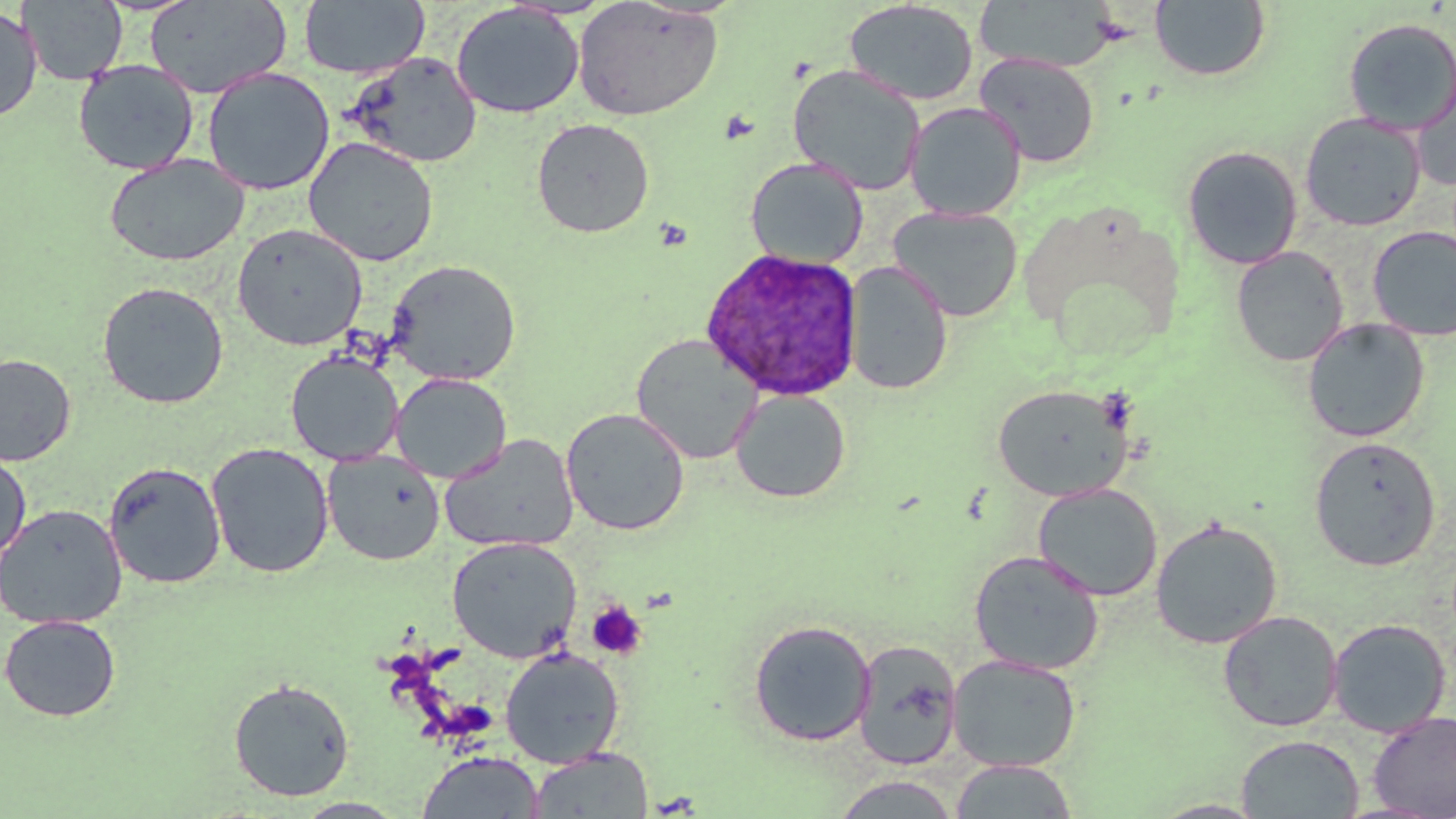
Approximate bounding boxes as named x1/y1/x2/y2 corners in pixels. Uninfected red blood cell locations: (x1=19, y1=0, x2=127, y2=86), (x1=300, y1=0, x2=429, y2=79), (x1=571, y1=0, x2=724, y2=121), (x1=1149, y1=0, x2=1271, y2=81), (x1=145, y1=1, x2=290, y2=98), (x1=843, y1=1, x2=979, y2=106), (x1=973, y1=1, x2=1121, y2=74), (x1=451, y1=3, x2=585, y2=119), (x1=0, y1=7, x2=42, y2=123), (x1=1342, y1=17, x2=1456, y2=134), (x1=347, y1=52, x2=482, y2=168), (x1=975, y1=53, x2=1099, y2=168), (x1=73, y1=59, x2=199, y2=175), (x1=1411, y1=63, x2=1456, y2=190), (x1=788, y1=64, x2=926, y2=196), (x1=202, y1=67, x2=335, y2=196), (x1=904, y1=102, x2=1026, y2=221), (x1=1299, y1=112, x2=1427, y2=232), (x1=531, y1=118, x2=655, y2=238), (x1=303, y1=136, x2=439, y2=267), (x1=1182, y1=145, x2=1303, y2=269), (x1=104, y1=153, x2=250, y2=266), (x1=745, y1=157, x2=869, y2=269), (x1=888, y1=206, x2=1023, y2=322), (x1=232, y1=223, x2=367, y2=350), (x1=1367, y1=225, x2=1456, y2=341), (x1=1230, y1=246, x2=1349, y2=366), (x1=385, y1=258, x2=522, y2=385), (x1=844, y1=262, x2=953, y2=396), (x1=96, y1=281, x2=229, y2=409), (x1=1302, y1=317, x2=1430, y2=443), (x1=631, y1=333, x2=763, y2=465), (x1=285, y1=350, x2=403, y2=466), (x1=0, y1=352, x2=76, y2=467), (x1=391, y1=372, x2=511, y2=484), (x1=992, y1=383, x2=1135, y2=501), (x1=730, y1=389, x2=850, y2=503), (x1=560, y1=408, x2=690, y2=536), (x1=439, y1=433, x2=579, y2=554), (x1=1309, y1=435, x2=1441, y2=571), (x1=206, y1=442, x2=334, y2=579), (x1=0, y1=449, x2=31, y2=566), (x1=322, y1=450, x2=446, y2=566), (x1=104, y1=461, x2=226, y2=590), (x1=1032, y1=483, x2=1163, y2=601), (x1=0, y1=503, x2=127, y2=630), (x1=1150, y1=517, x2=1283, y2=649), (x1=446, y1=535, x2=581, y2=663), (x1=968, y1=550, x2=1105, y2=675), (x1=1218, y1=610, x2=1342, y2=732), (x1=0, y1=613, x2=122, y2=722), (x1=1327, y1=618, x2=1452, y2=737), (x1=748, y1=619, x2=876, y2=747), (x1=852, y1=640, x2=962, y2=771), (x1=500, y1=647, x2=624, y2=768), (x1=947, y1=654, x2=1081, y2=772), (x1=228, y1=678, x2=355, y2=801), (x1=1368, y1=711, x2=1456, y2=818), (x1=1235, y1=734, x2=1364, y2=818), (x1=527, y1=747, x2=653, y2=818), (x1=416, y1=751, x2=545, y2=819), (x1=949, y1=759, x2=1078, y2=818), (x1=832, y1=774, x2=960, y2=818), (x1=291, y1=798, x2=409, y2=818), (x1=1148, y1=799, x2=1270, y2=818). Plasmodium ovale-infected red blood cell locations: (x1=699, y1=250, x2=863, y2=405). Platelet locations: (x1=586, y1=599, x2=647, y2=660). Slide-level diagnosis: Plasmodium ovale. Thin blood smear. Single field of view. Image is 1456×819 pixels. Captured at 1000x magnification. May-Grünwald-Giemsa stain. Optical microscopy.